Report the malaria status of this cell.
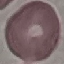
It is uninfected.

Summary:
  - Preparation: thin smear
  - Stain: Giemsa
  - Capture: smartphone camera at the microscope eyepiece
  - Image type: automatically extracted cell patch, resized to 64 × 64 pixels